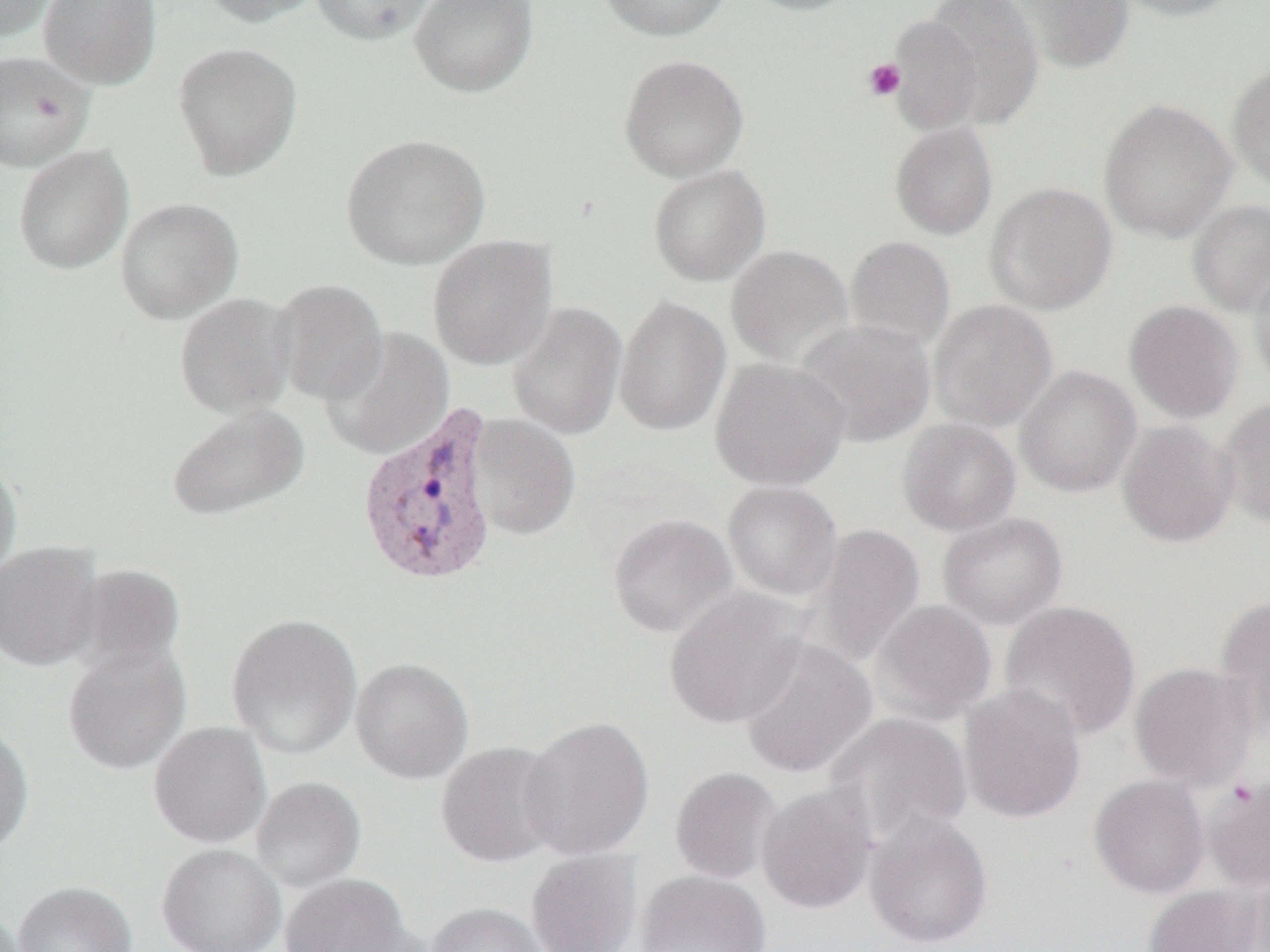
Approximate bounding boxes as (x1,y1)-(x2,y2) corner pairs in pixels. Uninfected red blood cell locations: (0,0)-(59,41), (39,0)-(163,90), (197,0)-(326,27), (310,0)-(438,45), (410,0)-(539,98), (596,0)-(731,41), (739,0)-(862,16), (921,0)-(1045,131), (1004,0)-(1135,74), (1111,0)-(1244,21), (887,14)-(985,133), (172,41)-(303,180), (0,50)-(93,171), (618,53)-(750,182), (1227,62)-(1270,192), (1098,97)-(1237,243), (889,121)-(998,240), (341,132)-(491,271), (13,144)-(134,274), (647,164)-(772,286), (984,182)-(1117,315), (115,197)-(243,323), (1187,199)-(1270,316), (427,235)-(557,371), (845,235)-(956,352), (725,244)-(854,367), (1250,264)-(1270,394), (271,279)-(389,405), (174,293)-(297,418), (614,294)-(731,437), (929,299)-(1057,432), (1124,299)-(1244,424), (507,300)-(628,440), (795,319)-(936,447), (320,327)-(455,459), (709,357)-(851,491), (1015,365)-(1142,497), (1217,396)-(1270,529), (166,403)-(309,521), (467,414)-(581,541), (897,418)-(1022,536), (1116,420)-(1237,548), (0,458)-(22,581), (722,480)-(843,602), (938,512)-(1068,629), (607,513)-(736,637), (810,522)-(926,666), (0,542)-(104,672), (73,563)-(186,673), (664,588)-(809,729), (1213,597)-(1270,740), (869,599)-(998,726), (999,600)-(1141,742), (226,613)-(363,759), (738,637)-(878,778), (62,642)-(191,775), (350,657)-(474,784), (1128,661)-(1260,791), (958,683)-(1087,824), (826,712)-(974,845), (518,715)-(655,861), (0,719)-(34,854), (148,722)-(272,848), (435,741)-(565,867), (670,767)-(782,884), (1088,774)-(1211,898), (251,776)-(366,892), (1203,776)-(1270,893), (757,784)-(878,915), (864,811)-(994,949), (157,843)-(286,952), (525,849)-(641,952), (636,869)-(772,952), (280,873)-(412,952), (1230,874)-(1270,951), (13,881)-(137,952), (1143,884)-(1263,952), (425,903)-(551,952), (0,907)-(27,952). Platelet locations: (862,58)-(906,101). Plasmodium vivax-infected red blood cell locations: (355,405)-(501,590). Slide-level diagnosis: Plasmodium vivax. Image is 1270×952 pixels. Thin blood film. 1000x magnification. Single field of view. Optical microscopy.